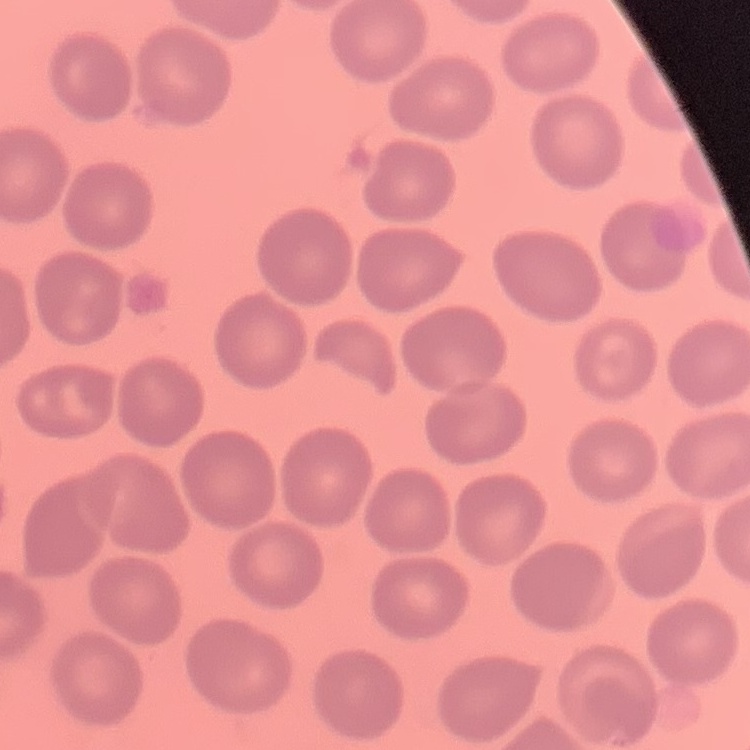
Summary:
  - Red blood cell morphology: no rouleaux formation
  - Image type: square crop of a larger photomicrograph
  - Stain: Field's or Giemsa
  - Preparation: thin blood film